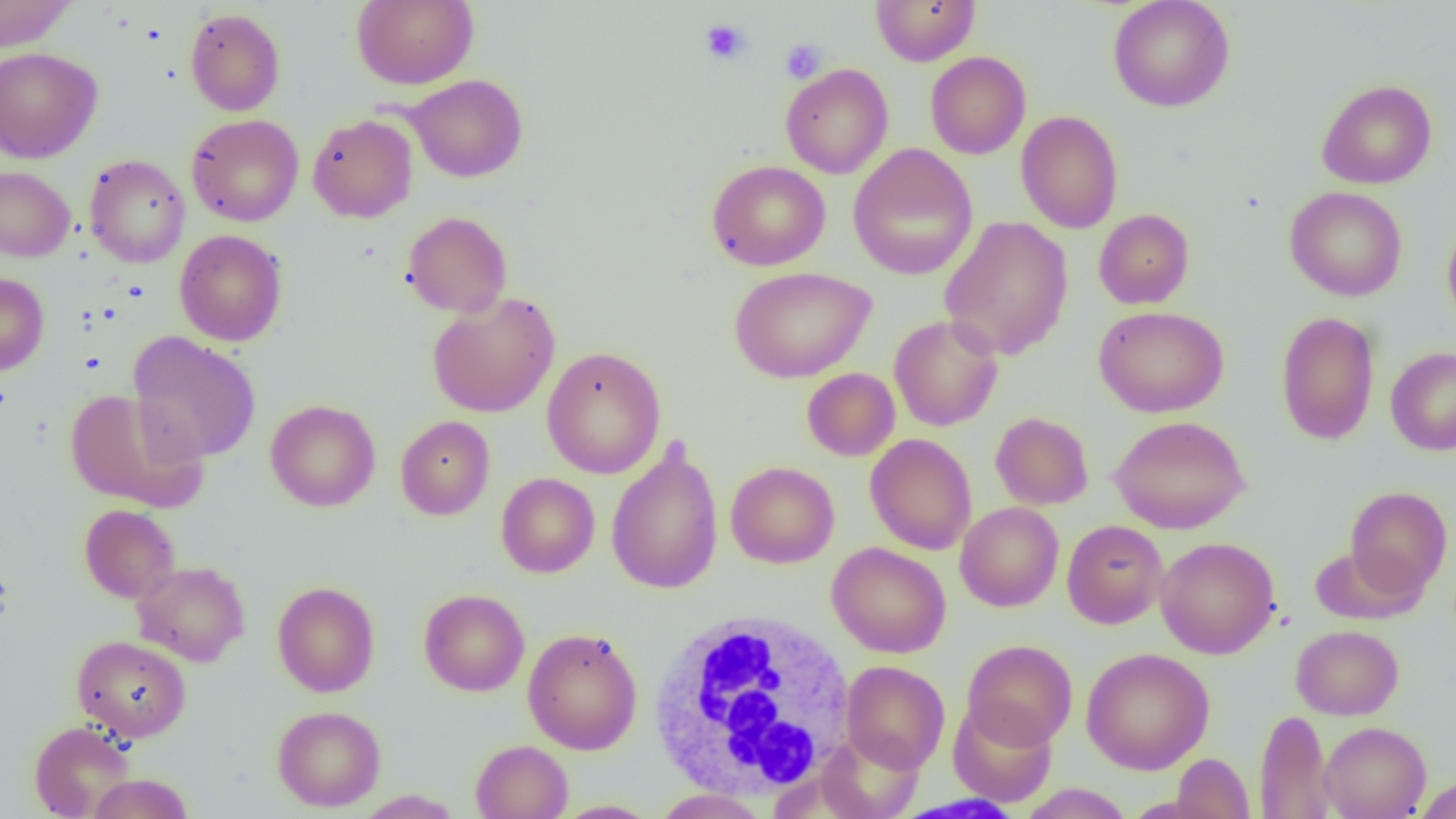

Approximate bounding boxes as [x1, y1, x2, y2] in pixels. Platelet locations: [700, 19, 752, 64], [780, 39, 827, 83]. White blood cell locations: [646, 610, 858, 799]. Uninfected red blood cell locations: [0, 0, 78, 51], [351, 0, 479, 89], [870, 0, 981, 66], [1107, 0, 1235, 112], [184, 8, 285, 116], [0, 46, 102, 163], [925, 51, 1030, 159], [780, 63, 893, 178], [405, 74, 528, 182], [1316, 79, 1438, 189], [1016, 110, 1123, 233], [186, 114, 304, 226], [307, 114, 418, 223], [848, 143, 978, 281], [84, 154, 190, 268], [706, 160, 831, 271], [0, 165, 75, 261], [1285, 186, 1407, 301], [1094, 209, 1194, 309], [402, 211, 512, 318], [939, 216, 1074, 360], [1442, 218, 1456, 334], [174, 229, 288, 346], [729, 266, 876, 383], [0, 272, 49, 375], [427, 291, 560, 418], [1094, 306, 1228, 417], [1276, 311, 1381, 445], [889, 315, 1003, 431], [127, 333, 261, 464], [542, 346, 666, 479], [1386, 347, 1456, 456], [802, 368, 900, 461], [64, 389, 208, 513], [265, 399, 381, 512], [990, 411, 1094, 510], [396, 415, 495, 520], [1109, 415, 1251, 534], [865, 433, 977, 554], [606, 439, 723, 596], [725, 461, 839, 568], [496, 473, 600, 578], [1345, 486, 1453, 598], [955, 502, 1064, 612], [79, 504, 180, 602], [1062, 520, 1168, 629], [1156, 536, 1280, 659], [827, 541, 951, 658], [1309, 546, 1428, 625], [132, 561, 250, 667], [272, 581, 380, 697], [419, 588, 530, 696], [1291, 624, 1404, 720], [523, 627, 642, 755], [71, 635, 192, 742], [963, 639, 1077, 750], [1082, 647, 1215, 774], [841, 660, 950, 773], [948, 700, 1057, 807], [272, 705, 386, 811], [1254, 709, 1334, 819], [28, 720, 136, 818], [1318, 721, 1431, 819], [816, 730, 923, 819], [471, 740, 573, 819], [1172, 753, 1255, 818], [87, 773, 194, 818], [1412, 776, 1456, 819], [1017, 783, 1134, 818], [654, 788, 768, 819], [352, 790, 463, 818], [551, 800, 661, 818]. Slide-level diagnosis: negative for blood parasites. Single field of view. Image is 1456×819 pixels. Thin blood film. Captured at 1000x magnification. Optical microscopy.